Outline each P. falciparum parasite and classify it by life-cycle stage.
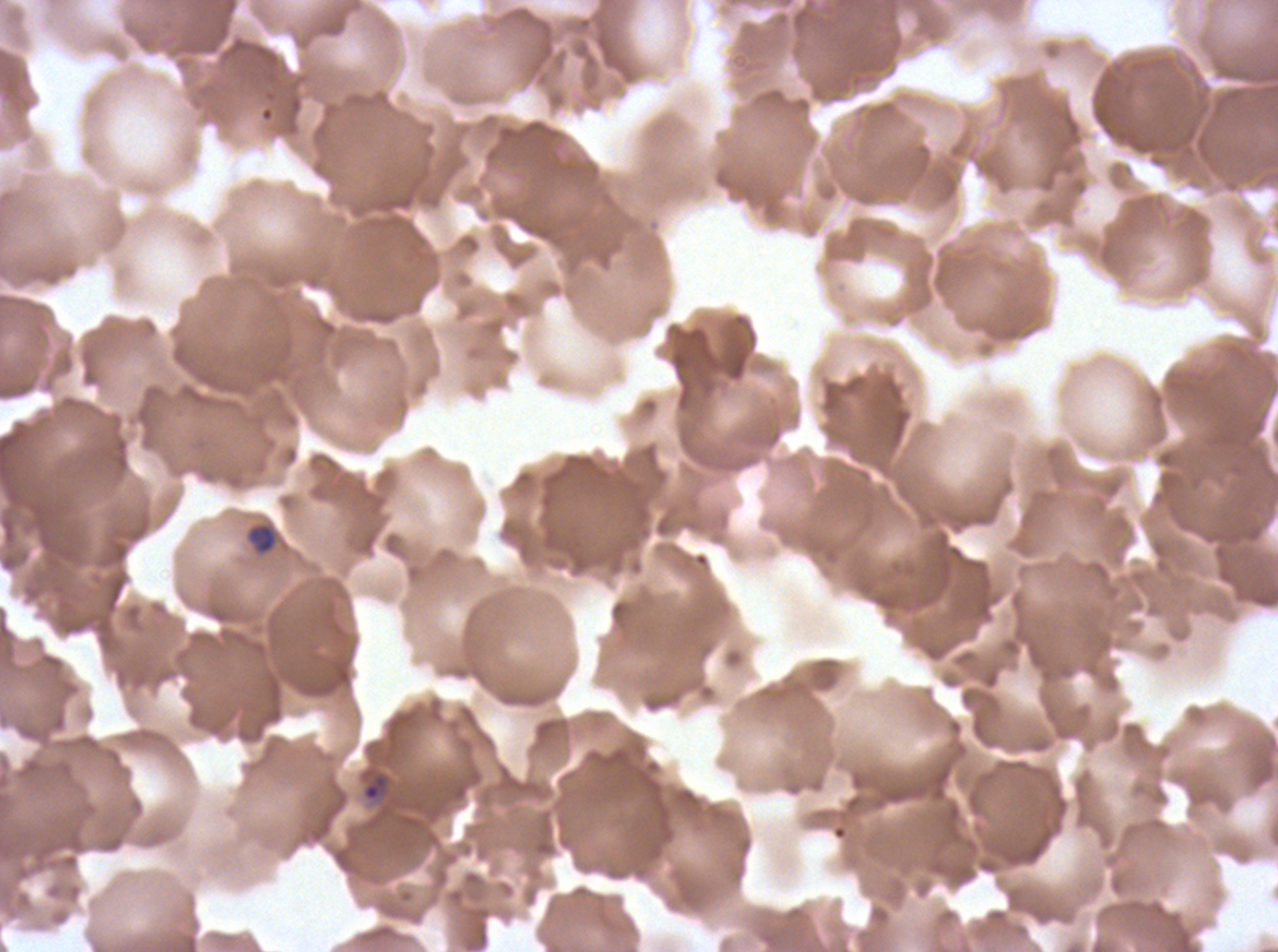
Approximate bounding boxes as {x1, y1, x2, y2} in pixels.
Rings: {361, 772, 389, 802}.
Late-ring/early-trophozoite forms: {249, 524, 276, 554}.
No mid trophozoites, late trophozoites, early schizonts, late schizonts, segmenters, or gametocytes observed.

Summary:
  - Stain: Giemsa
  - Preparation: thin blood smear
  - Image size: 1278×952 pixels
  - Life-cycle stages observed: ring, late-ring/early-trophozoite
  - Specimen: P. falciparum from a patient in The Gambia, cultured ex vivo for 24 to 48 hours
  - Field of view: one sub-image of a larger composite